Identify the parasite.
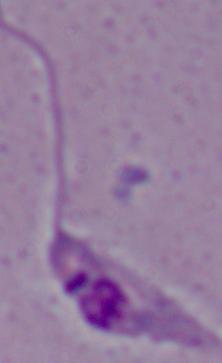
This is Leishmania.

{
  "modality": "photomicrograph",
  "magnification": "1000x"
}